Assess the morphology of the red blood cells.
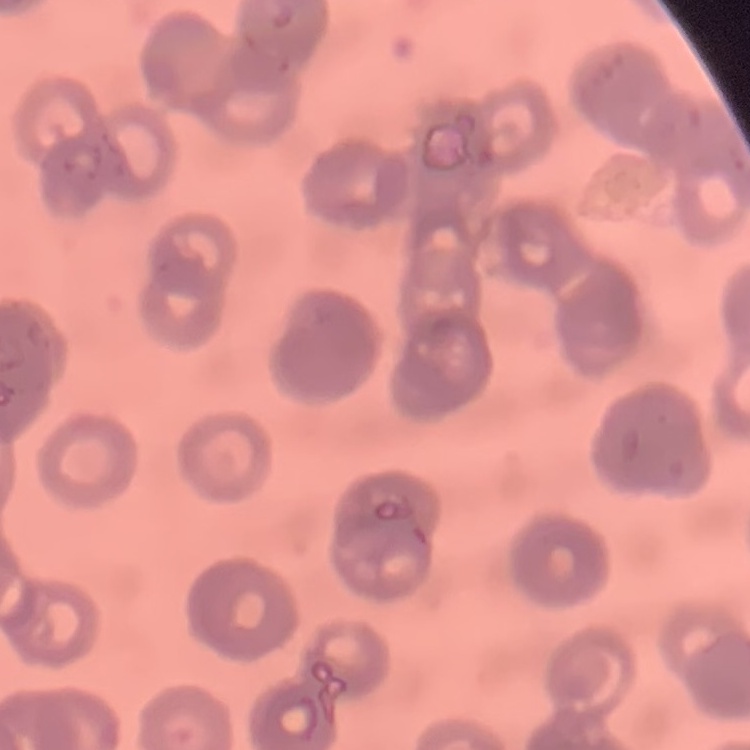

Rouleaux formation.

{
  "image_type": "one tile cut from a larger photomicrograph",
  "stain": "Field's or Giemsa",
  "preparation": "thin peripheral smear"
}